Locate every blood parasite and identify its species.
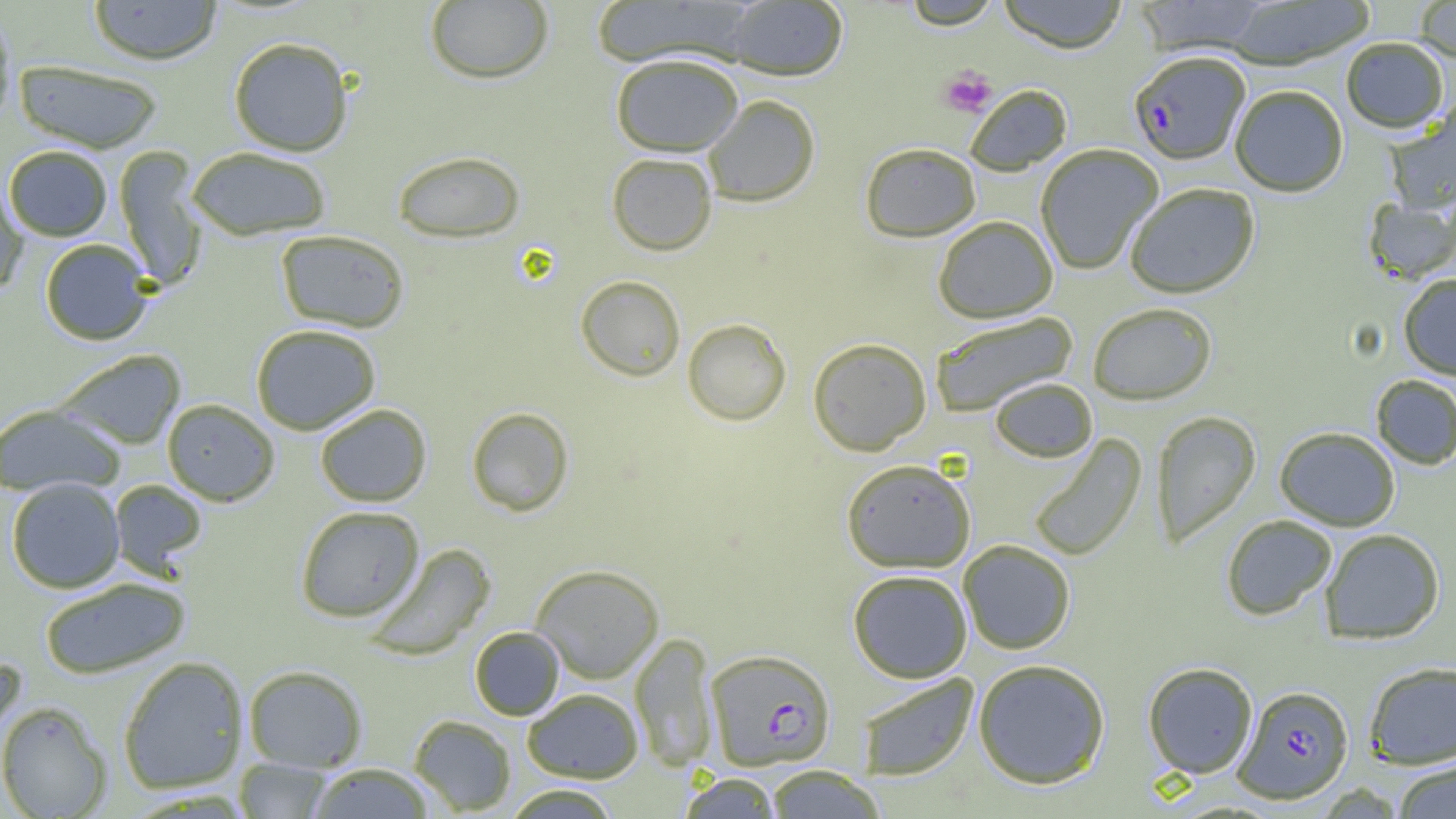
Approximate bounding boxes as named x1/y1/x2/y2 corners in pixels.
Plasmodium falciparum-infected red blood cells: (x1=1129, y1=50, x2=1250, y2=165), (x1=705, y1=649, x2=835, y2=771), (x1=1233, y1=685, x2=1354, y2=803).
No Plasmodium ovale, Plasmodium malariae, Plasmodium vivax, Babesia divergens, or Trypanosoma brucei observed.

slide-level diagnosis = Plasmodium falciparum
uninfected red blood cell locations = approximate bounding boxes as named x1/y1/x2/y2 corners in pixels: (x1=88, y1=0, x2=222, y2=64), (x1=590, y1=0, x2=754, y2=68), (x1=899, y1=0, x2=1002, y2=30), (x1=997, y1=0, x2=1129, y2=54), (x1=1134, y1=0, x2=1271, y2=55), (x1=1222, y1=0, x2=1376, y2=70), (x1=425, y1=1, x2=554, y2=84), (x1=725, y1=1, x2=848, y2=81), (x1=1412, y1=1, x2=1456, y2=63), (x1=0, y1=11, x2=16, y2=130), (x1=228, y1=37, x2=354, y2=156), (x1=1341, y1=39, x2=1449, y2=135), (x1=610, y1=53, x2=744, y2=156), (x1=13, y1=59, x2=163, y2=154), (x1=965, y1=84, x2=1072, y2=175), (x1=1230, y1=85, x2=1348, y2=197), (x1=702, y1=94, x2=821, y2=206), (x1=1385, y1=105, x2=1456, y2=215), (x1=860, y1=142, x2=981, y2=242), (x1=1035, y1=144, x2=1163, y2=274), (x1=3, y1=145, x2=113, y2=241), (x1=113, y1=146, x2=207, y2=291), (x1=186, y1=146, x2=332, y2=240), (x1=392, y1=150, x2=525, y2=243), (x1=606, y1=152, x2=717, y2=255), (x1=0, y1=179, x2=29, y2=296), (x1=1124, y1=183, x2=1260, y2=299), (x1=1363, y1=196, x2=1455, y2=286), (x1=933, y1=215, x2=1058, y2=323), (x1=275, y1=229, x2=410, y2=333), (x1=40, y1=239, x2=153, y2=345), (x1=1398, y1=274, x2=1456, y2=380), (x1=575, y1=275, x2=686, y2=381), (x1=1087, y1=302, x2=1217, y2=405), (x1=929, y1=311, x2=1078, y2=416), (x1=682, y1=318, x2=791, y2=426), (x1=250, y1=323, x2=381, y2=435), (x1=808, y1=337, x2=931, y2=456), (x1=55, y1=349, x2=187, y2=450), (x1=1371, y1=375, x2=1456, y2=470), (x1=990, y1=377, x2=1097, y2=462), (x1=161, y1=398, x2=280, y2=506), (x1=0, y1=403, x2=126, y2=497), (x1=314, y1=403, x2=432, y2=507), (x1=466, y1=406, x2=574, y2=516), (x1=1151, y1=410, x2=1261, y2=548), (x1=1275, y1=426, x2=1400, y2=531), (x1=1028, y1=434, x2=1147, y2=562), (x1=841, y1=458, x2=976, y2=573), (x1=6, y1=477, x2=125, y2=593), (x1=108, y1=479, x2=208, y2=578), (x1=295, y1=505, x2=425, y2=622), (x1=1221, y1=515, x2=1337, y2=621), (x1=1319, y1=528, x2=1445, y2=644), (x1=958, y1=540, x2=1075, y2=655), (x1=365, y1=543, x2=496, y2=660), (x1=530, y1=563, x2=664, y2=683), (x1=847, y1=569, x2=973, y2=683), (x1=38, y1=576, x2=191, y2=679), (x1=469, y1=626, x2=564, y2=720), (x1=630, y1=632, x2=718, y2=773), (x1=0, y1=654, x2=25, y2=745), (x1=117, y1=656, x2=249, y2=794), (x1=972, y1=658, x2=1111, y2=789), (x1=1363, y1=661, x2=1456, y2=769), (x1=1142, y1=662, x2=1259, y2=779), (x1=243, y1=665, x2=368, y2=772), (x1=856, y1=673, x2=979, y2=781), (x1=523, y1=688, x2=643, y2=783), (x1=0, y1=701, x2=112, y2=818), (x1=409, y1=714, x2=517, y2=815), (x1=234, y1=758, x2=334, y2=818), (x1=1391, y1=760, x2=1456, y2=818), (x1=306, y1=763, x2=435, y2=818), (x1=761, y1=765, x2=887, y2=818), (x1=679, y1=773, x2=783, y2=819), (x1=500, y1=784, x2=622, y2=819)
platelet locations = approximate bounding boxes as named x1/y1/x2/y2 corners in pixels: (x1=938, y1=66, x2=997, y2=118)
field of view = single
preparation = thin blood film
modality = optical microscopy
magnification = 1000x
image size = 1456×819 pixels